Locate every blood parasite and identify its species.
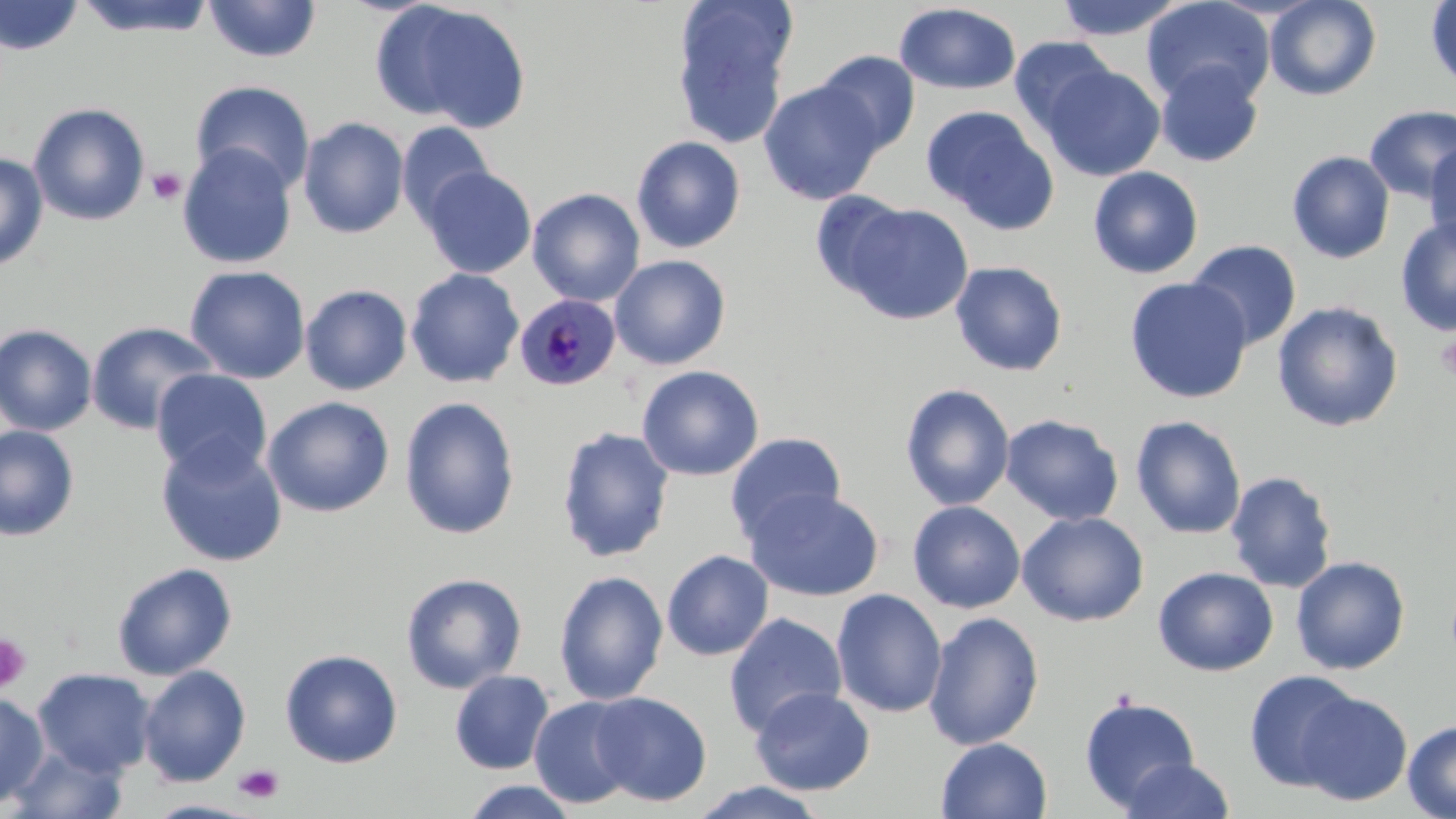
Approximate bounding boxes as named x1/y1/x2/y2 corners in pixels.
Plasmodium malariae-infected red blood cells: (x1=515, y1=294, x2=621, y2=391).
No Plasmodium falciparum, Plasmodium ovale, Plasmodium vivax, Babesia divergens, or Trypanosoma brucei observed.

Platelet locations: (x1=147, y1=167, x2=187, y2=205), (x1=1436, y1=333, x2=1456, y2=381), (x1=0, y1=634, x2=32, y2=694), (x1=233, y1=763, x2=284, y2=803). Uninfected red blood cell locations: (x1=0, y1=0, x2=83, y2=56), (x1=73, y1=0, x2=219, y2=38), (x1=203, y1=0, x2=321, y2=63), (x1=1052, y1=0, x2=1187, y2=41), (x1=1142, y1=0, x2=1275, y2=108), (x1=1264, y1=0, x2=1381, y2=101), (x1=1425, y1=0, x2=1456, y2=94), (x1=377, y1=2, x2=531, y2=132), (x1=671, y1=2, x2=797, y2=149), (x1=893, y1=3, x2=1022, y2=95), (x1=1009, y1=36, x2=1118, y2=139), (x1=814, y1=50, x2=920, y2=155), (x1=1155, y1=62, x2=1264, y2=167), (x1=1041, y1=63, x2=1166, y2=181), (x1=189, y1=80, x2=316, y2=196), (x1=758, y1=80, x2=885, y2=205), (x1=28, y1=102, x2=151, y2=226), (x1=1363, y1=104, x2=1456, y2=204), (x1=920, y1=105, x2=1059, y2=234), (x1=297, y1=117, x2=409, y2=239), (x1=397, y1=121, x2=495, y2=228), (x1=630, y1=135, x2=747, y2=253), (x1=1425, y1=139, x2=1456, y2=249), (x1=177, y1=144, x2=298, y2=270), (x1=1287, y1=150, x2=1395, y2=264), (x1=0, y1=153, x2=50, y2=273), (x1=1088, y1=166, x2=1204, y2=279), (x1=422, y1=167, x2=536, y2=279), (x1=527, y1=188, x2=645, y2=306), (x1=810, y1=190, x2=912, y2=299), (x1=840, y1=203, x2=973, y2=324), (x1=1395, y1=215, x2=1455, y2=337), (x1=1186, y1=239, x2=1302, y2=351), (x1=610, y1=254, x2=731, y2=370), (x1=950, y1=260, x2=1068, y2=376), (x1=184, y1=265, x2=311, y2=384), (x1=405, y1=268, x2=524, y2=389), (x1=1124, y1=277, x2=1253, y2=403), (x1=300, y1=284, x2=413, y2=395), (x1=1272, y1=300, x2=1404, y2=432), (x1=86, y1=321, x2=219, y2=434), (x1=0, y1=323, x2=97, y2=435), (x1=636, y1=365, x2=764, y2=481), (x1=152, y1=369, x2=272, y2=482), (x1=900, y1=383, x2=1015, y2=510), (x1=262, y1=396, x2=395, y2=517), (x1=399, y1=396, x2=520, y2=540), (x1=1000, y1=413, x2=1125, y2=526), (x1=1130, y1=415, x2=1247, y2=540), (x1=0, y1=425, x2=80, y2=541), (x1=556, y1=427, x2=675, y2=563), (x1=724, y1=432, x2=848, y2=545), (x1=155, y1=439, x2=288, y2=567), (x1=1225, y1=470, x2=1338, y2=594), (x1=744, y1=487, x2=884, y2=601), (x1=908, y1=500, x2=1026, y2=613), (x1=1016, y1=511, x2=1149, y2=627), (x1=661, y1=550, x2=774, y2=661), (x1=1290, y1=556, x2=1410, y2=675), (x1=111, y1=562, x2=237, y2=681), (x1=1153, y1=567, x2=1279, y2=676), (x1=553, y1=570, x2=669, y2=706), (x1=400, y1=572, x2=528, y2=694), (x1=831, y1=588, x2=947, y2=718), (x1=723, y1=612, x2=847, y2=738), (x1=923, y1=612, x2=1045, y2=749), (x1=280, y1=648, x2=403, y2=768), (x1=138, y1=665, x2=250, y2=787), (x1=33, y1=669, x2=156, y2=777), (x1=449, y1=670, x2=555, y2=774), (x1=1244, y1=670, x2=1363, y2=792), (x1=750, y1=687, x2=875, y2=796), (x1=588, y1=691, x2=712, y2=806), (x1=1297, y1=691, x2=1412, y2=806), (x1=0, y1=692, x2=49, y2=807), (x1=1078, y1=695, x2=1200, y2=812), (x1=529, y1=696, x2=641, y2=809), (x1=1403, y1=719, x2=1456, y2=819), (x1=936, y1=737, x2=1052, y2=819), (x1=6, y1=743, x2=130, y2=819), (x1=1119, y1=757, x2=1236, y2=818), (x1=461, y1=779, x2=579, y2=818), (x1=689, y1=781, x2=831, y2=818). Slide-level diagnosis: Plasmodium malariae. Light microscopy. 1000x magnification. Image is 1456×819 pixels. One field of a larger specimen. Thin blood smear. May-Grünwald-Giemsa-stained preparation.